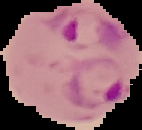
result: Plasmodium parasites detected
image_size: 142×130 pixels
image_type: segmented cell region on a black background
preparation: thin blood smear